Identify the parasite.
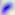

Toxoplasma gondii.

Photomicrograph. Captured at 400x magnification.